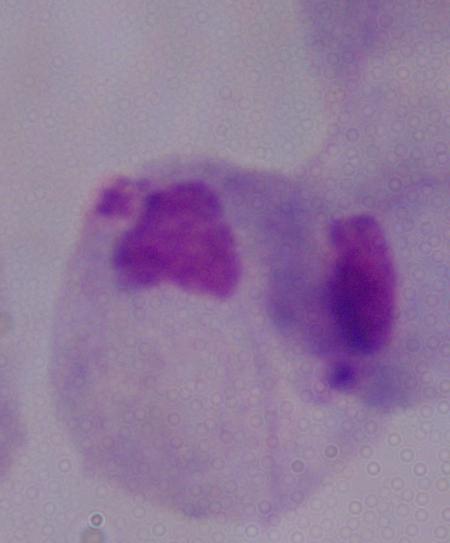 1000x magnification. Photomicrograph. A trichomonad is shown.